Assess this cell for malaria.
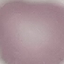
It is uninfected.

capture = smartphone camera at the microscope eyepiece
preparation = thin blood film
image type = automatically extracted cell patch, resized to 64 × 64 pixels
stain = Giemsa